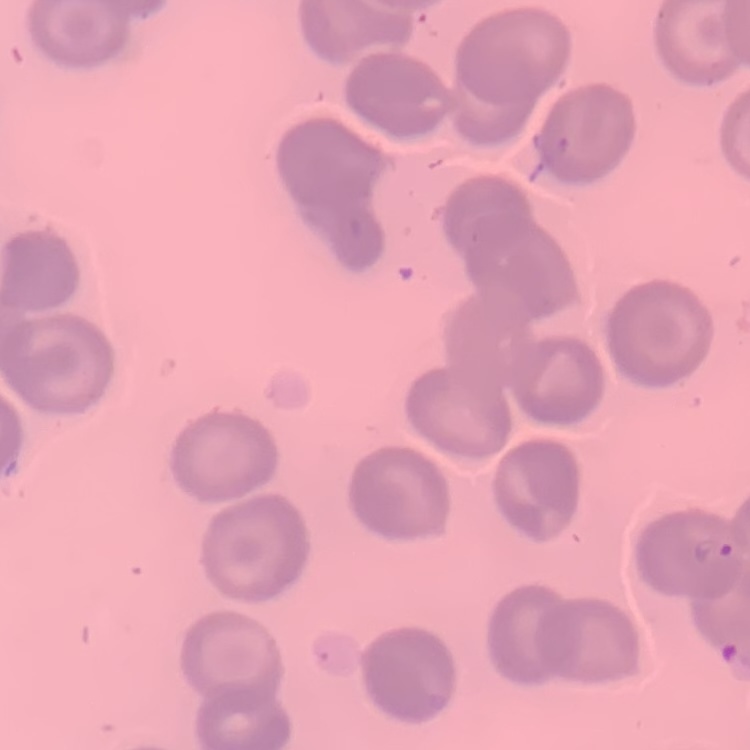
Summary:
  - Erythrocyte morphology: no rouleaux formation
  - Image type: square crop of a larger photomicrograph
  - Preparation: thin peripheral smear
  - Stain: Field's or Giemsa